Report the malaria status of this cell.
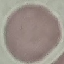

It is uninfected.

Summary:
  - Capture: smartphone through the microscope eyepiece
  - Image type: automatically extracted cell patch, resized to 64 × 64 pixels
  - Preparation: thin blood smear
  - Stain: Giemsa